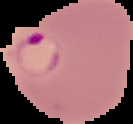

Malaria status: parasitized. The area outside the segmented cell region is set to black. Image is 133×124 pixels. From a thin blood film.